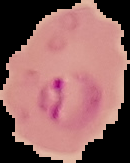
preparation = thin blood smear
result = Plasmodium parasites identified
image type = cell region segmented out of the field of view; surrounding area masked to black
image size = 130×163 pixels